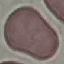

result = no malaria parasites detected
capture = smartphone through the microscope eyepiece
preparation = thin blood film
image type = automatically extracted cell patch, resized to 64 × 64 pixels
stain = Giemsa